Give the extent of all Plasmodium malariae-infected red blood cells.
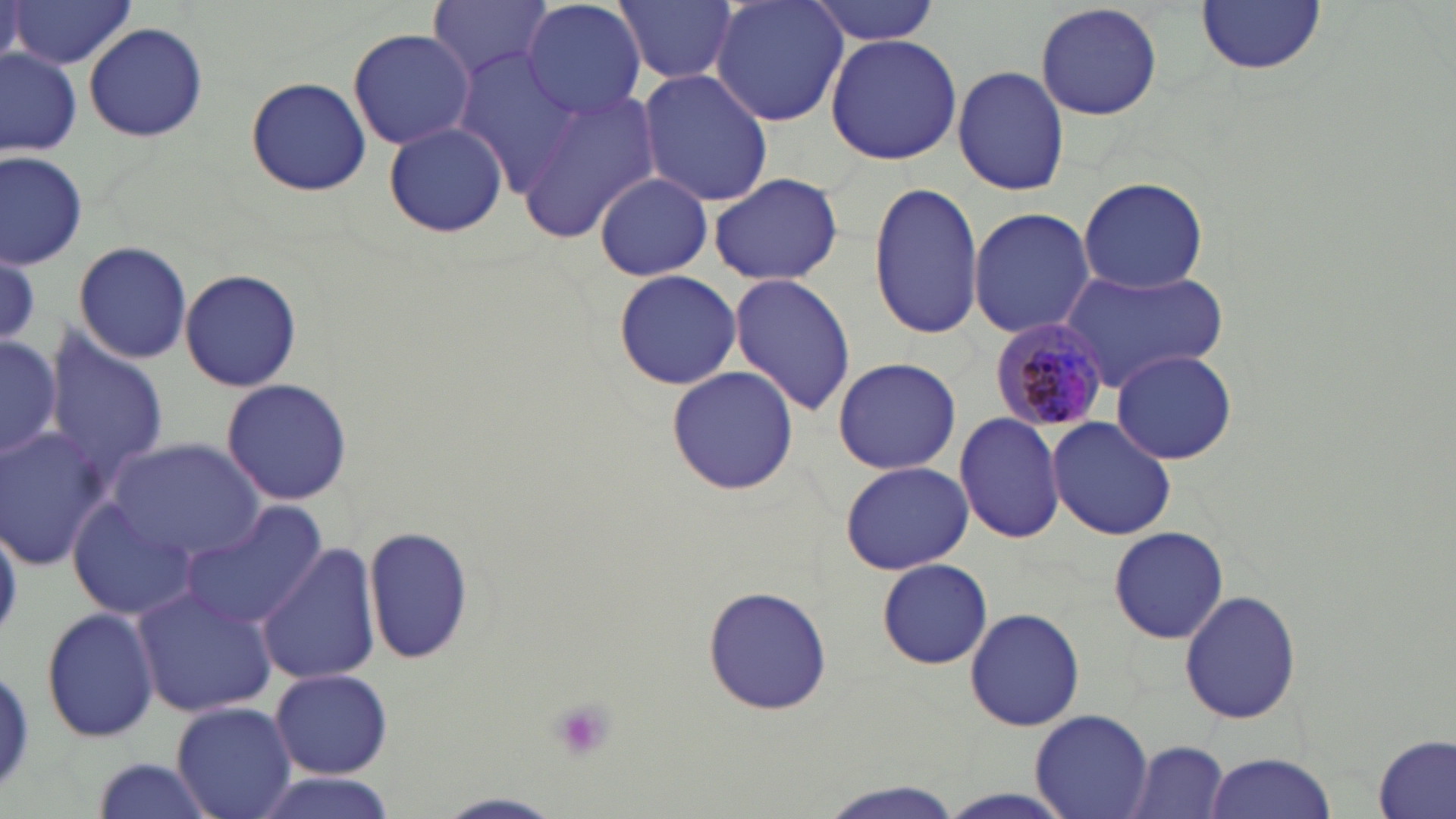
Approximate bounding boxes as (x1, y1, x2, y2) in pixels.
Plasmodium malariae-infected red blood cells: (988, 319, 1110, 434).

Uninfected red blood cell locations: (5, 0, 138, 70), (427, 0, 554, 82), (520, 0, 648, 119), (615, 0, 736, 85), (711, 0, 848, 126), (807, 0, 945, 46), (1197, 0, 1326, 76), (1033, 1, 1164, 122), (83, 23, 210, 141), (347, 26, 477, 151), (825, 32, 961, 166), (0, 49, 80, 156), (451, 50, 593, 197), (953, 63, 1068, 197), (635, 67, 773, 208), (246, 76, 372, 197), (516, 88, 663, 243), (383, 122, 508, 238), (0, 151, 87, 270), (593, 172, 715, 278), (707, 172, 844, 285), (1077, 176, 1209, 293), (867, 183, 985, 338), (967, 206, 1096, 339), (74, 240, 192, 363), (71, 250, 299, 376), (0, 252, 41, 345), (1057, 267, 1229, 392), (179, 269, 304, 392), (612, 269, 741, 390), (728, 273, 857, 416), (1, 328, 62, 464), (41, 333, 170, 489), (1111, 350, 1239, 464), (832, 356, 961, 476), (666, 366, 800, 495), (221, 378, 353, 504), (954, 412, 1066, 543), (1046, 416, 1176, 539), (0, 427, 108, 570), (110, 436, 267, 566), (838, 460, 974, 574), (67, 498, 194, 621), (182, 500, 327, 632), (1, 514, 21, 643), (363, 524, 474, 665), (1109, 527, 1230, 644), (257, 541, 379, 686), (878, 558, 992, 669), (134, 583, 278, 718), (702, 587, 833, 717), (1179, 589, 1303, 726), (40, 606, 158, 745), (962, 606, 1086, 733), (0, 657, 35, 800), (270, 668, 391, 779), (172, 702, 296, 819), (1031, 709, 1152, 819), (1375, 736, 1455, 819), (1122, 739, 1233, 819), (1201, 751, 1338, 819), (93, 756, 212, 818), (250, 774, 397, 818), (814, 778, 966, 819), (440, 791, 563, 817). Platelet locations: (548, 698, 616, 763). Slide-level diagnosis: Plasmodium malariae. May-Grünwald-Giemsa stain. Light microscopy. Image is 1456×819 pixels. 1000x magnification. Thin blood film. One field of a larger specimen.